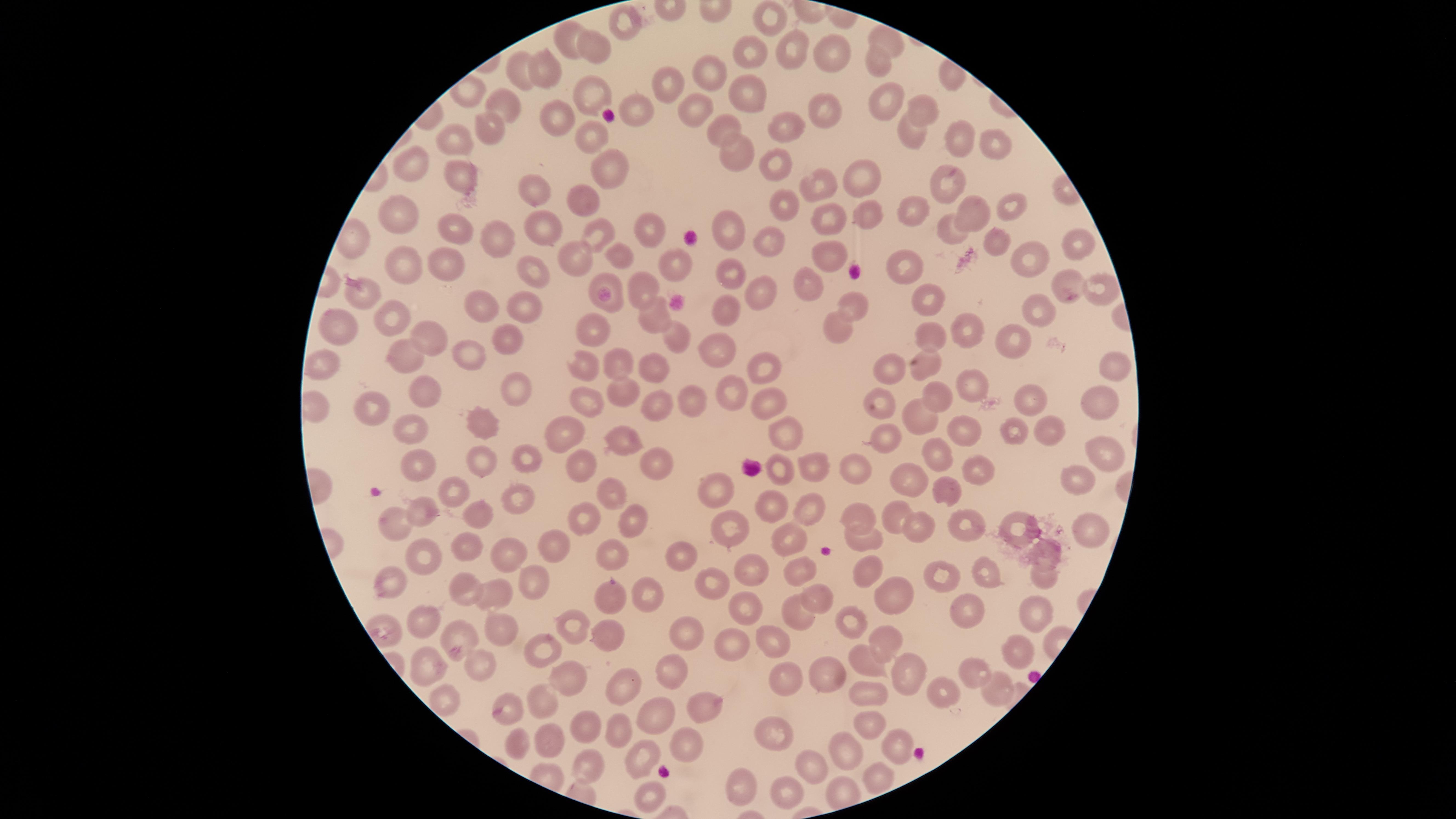

Approximate marker points as {x, y} in pixels.
Summary:
  - Uninfected red blood cells: {772, 15}, {626, 28}, {571, 36}, {888, 39}, {795, 48}, {595, 50}, {834, 50}, {754, 51}, {878, 63}, {539, 70}, {705, 71}, {520, 73}, {667, 80}, {746, 88}, {888, 90}, {591, 91}, {508, 98}, {693, 104}, {828, 108}, {636, 109}, {926, 111}, {554, 115}, {788, 123}, {489, 124}, {718, 124}, {589, 130}, {916, 131}, {953, 136}, {993, 140}, {455, 142}, {733, 149}, {776, 157}, {410, 159}, {603, 166}, {467, 174}, {860, 176}, {947, 181}, {823, 184}, {538, 191}, {590, 193}, {784, 201}, {1010, 205}, {914, 209}, {972, 212}, {402, 214}, {867, 214}, {829, 216}, {550, 221}, {728, 224}, {653, 225}, {457, 227}, {953, 227}, {602, 229}, {993, 237}, {769, 238}, {501, 239}, {1081, 242}, {825, 251}, {579, 256}, {618, 256}, {444, 258}, {1029, 260}, {400, 264}, {902, 267}, {537, 270}, {734, 273}, {605, 281}, {813, 283}, {1072, 283}, {1103, 286}, {642, 287}, {761, 291}, {365, 292}, {929, 297}, {486, 302}, {851, 302}, {531, 304}, {728, 307}, {1035, 311}, {651, 313}, {393, 318}, {334, 325}, {593, 329}, {973, 330}, {841, 331}, {934, 333}, {674, 334}, {508, 335}, {428, 336}, {719, 343}, {1014, 343}, {471, 347}, {408, 356}, {631, 359}, {657, 362}, {322, 363}, {586, 364}, {889, 364}, {922, 365}, {1110, 366}, {761, 368}, {517, 384}, {973, 384}, {421, 387}, {621, 387}, {728, 388}, {944, 394}, {1030, 395}, {1093, 395}, {884, 397}, {693, 399}, {764, 400}, {589, 402}, {662, 405}, {376, 409}, {917, 412}, {479, 420}, {410, 422}, {963, 424}, {1049, 429}, {567, 430}, {1014, 431}, {791, 433}, {887, 434}, {622, 436}, {1097, 446}, {938, 450}, {661, 454}, {523, 459}, {417, 460}, {484, 461}, {579, 464}, {778, 464}, {810, 465}, {859, 468}, {980, 469}, {910, 474}, {1073, 482}, {947, 488}, {719, 490}, {612, 491}, {448, 492}, {517, 495}, {770, 506}, {810, 507}, {425, 511}, {474, 511}, {860, 511}, {899, 513}, {631, 516}, {1012, 516}, {577, 517}, {391, 524}, {727, 524}, {965, 524}, {924, 525}, {1093, 531}, {790, 535}, {862, 540}, {551, 543}, {465, 546}, {613, 547}, {678, 552}, {1045, 552}, {425, 554}, {504, 558}, {750, 564}, {798, 564}, {869, 568}, {986, 571}, {948, 572}, {1040, 576}, {533, 580}, {387, 582}, {708, 583}, {466, 589}, {497, 592}, {644, 594}, {813, 596}, {611, 597}, {893, 597}, {971, 601}, {742, 603}, {1032, 610}, {797, 611}, {853, 618}, {415, 620}, {572, 622}, {501, 623}, {606, 631}, {689, 631}, {458, 635}, {734, 637}, {884, 637}, {775, 644}, {1015, 644}, {540, 649}, {426, 659}, {859, 659}, {474, 666}, {674, 667}, {975, 668}, {824, 674}, {784, 675}, {569, 676}, {906, 676}, {617, 688}, {996, 688}, {940, 694}, {868, 695}, {445, 699}, {546, 700}, {510, 704}, {703, 705}, {658, 715}, {867, 721}, {590, 726}, {617, 731}, {776, 736}, {546, 737}, {684, 741}, {510, 743}, {895, 745}, {842, 751}, {643, 757}, {591, 765}, {814, 769}, {880, 775}, {738, 785}, {791, 788}, {649, 794}
  - Field of view: single
  - Preparation: thin smear of blood
  - Visible region: circular
  - Capture: smartphone photograph through the microscope eyepiece
  - Presence: no malaria parasites identified
  - Image size: 1456×819 pixels
  - Stain: Giemsa